Name the blood parasite species.
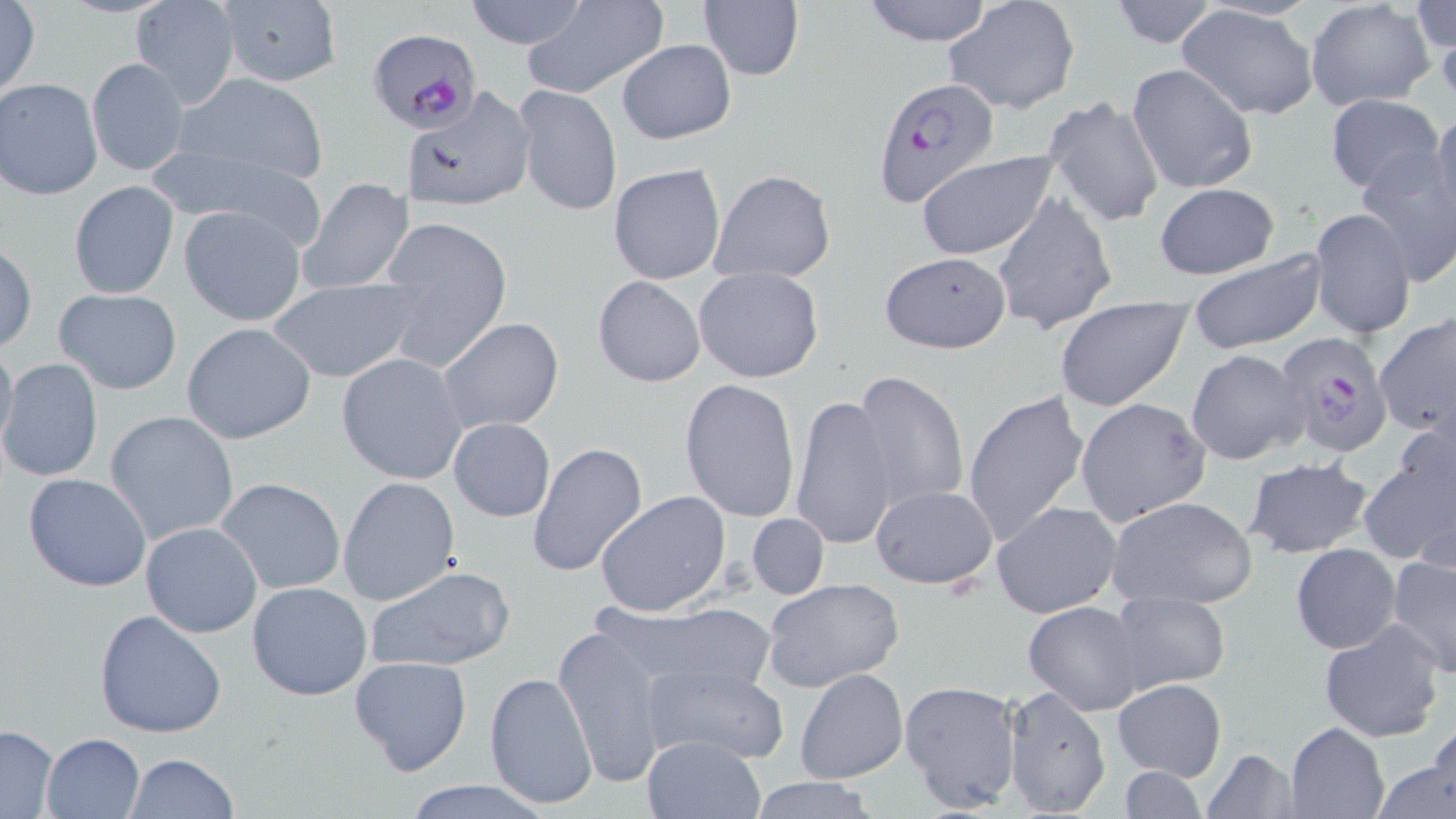
Plasmodium falciparum.

stain = May-Grünwald-Giemsa
preparation = thin blood film
image size = 1456×819 pixels
magnification = 1000x
Plasmodium falciparum-infected red blood cell locations = approximate bounding boxes as (x1, y1, x2, y2) in pixels: (368, 28, 483, 134), (871, 77, 1001, 209), (1276, 332, 1397, 458)
uninfected red blood cell locations = approximate bounding boxes as (x1, y1, x2, y2) in pixels: (463, 0, 591, 50), (521, 0, 670, 100), (859, 0, 998, 47), (943, 0, 1081, 114), (1107, 0, 1222, 49), (132, 1, 240, 109), (213, 1, 343, 88), (1305, 1, 1434, 111), (0, 2, 42, 100), (698, 2, 805, 81), (1412, 3, 1454, 55), (1176, 5, 1319, 121), (616, 38, 736, 145), (86, 57, 188, 177), (1127, 62, 1258, 195), (171, 72, 331, 185), (0, 77, 104, 200), (513, 84, 622, 216), (405, 85, 537, 212), (1042, 92, 1165, 229), (1326, 94, 1443, 196), (1428, 107, 1456, 228), (159, 146, 327, 247), (914, 149, 1062, 262), (1355, 149, 1456, 285), (608, 164, 726, 285), (709, 169, 837, 281), (298, 177, 415, 294), (68, 180, 180, 300), (1154, 183, 1279, 278), (992, 192, 1116, 336), (178, 204, 307, 326), (1308, 207, 1416, 340), (374, 215, 513, 373), (1, 241, 37, 353), (1188, 250, 1327, 353), (878, 252, 1011, 353), (693, 266, 824, 383), (592, 275, 707, 388), (268, 278, 418, 383), (52, 288, 183, 395), (1056, 295, 1193, 412), (1374, 314, 1456, 442), (438, 318, 564, 434), (181, 321, 318, 445), (0, 334, 18, 457), (1185, 348, 1310, 466), (337, 353, 469, 485), (0, 357, 104, 483), (853, 368, 969, 510), (679, 377, 801, 523), (961, 387, 1090, 548), (790, 395, 900, 552), (1076, 398, 1210, 524), (106, 411, 240, 543), (448, 417, 556, 522), (528, 441, 650, 580), (1358, 441, 1456, 572), (1243, 457, 1373, 561), (23, 472, 152, 593), (337, 476, 460, 607), (216, 477, 347, 594), (870, 484, 997, 589), (594, 491, 733, 616), (1106, 496, 1259, 608), (991, 499, 1123, 618), (747, 513, 828, 599), (141, 521, 263, 637), (1291, 542, 1401, 653), (1386, 553, 1456, 679), (364, 564, 516, 673), (760, 577, 907, 693), (246, 581, 374, 701), (1109, 590, 1232, 693), (613, 600, 778, 699), (1024, 601, 1144, 715), (93, 608, 227, 739), (1320, 621, 1445, 743), (554, 624, 669, 786), (348, 654, 472, 775), (642, 663, 788, 764), (794, 668, 907, 783), (483, 672, 598, 810), (1114, 677, 1227, 781), (899, 679, 1021, 812), (1001, 685, 1112, 819), (1420, 719, 1456, 811), (1285, 721, 1389, 819), (0, 725, 61, 816), (39, 731, 144, 817), (641, 734, 765, 819), (1200, 748, 1301, 818), (1376, 750, 1456, 819), (123, 753, 240, 819), (1117, 766, 1209, 819), (745, 777, 884, 817), (399, 778, 559, 819)
modality = optical microscopy
field of view = single